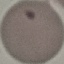

Result: negative for malaria parasites. Photographed with a smartphone camera at the microscope eyepiece. Automatically extracted cell patch, resized to 64 × 64 pixels. Thin blood smear. Giemsa stain.